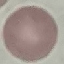
Summary:
  - Malaria status: uninfected
  - Image type: automatically extracted cell patch, resized to 64 × 64 pixels
  - Preparation: thin smear
  - Stain: Giemsa
  - Capture: smartphone through the microscope eyepiece